Outline each blood parasite and name the species.
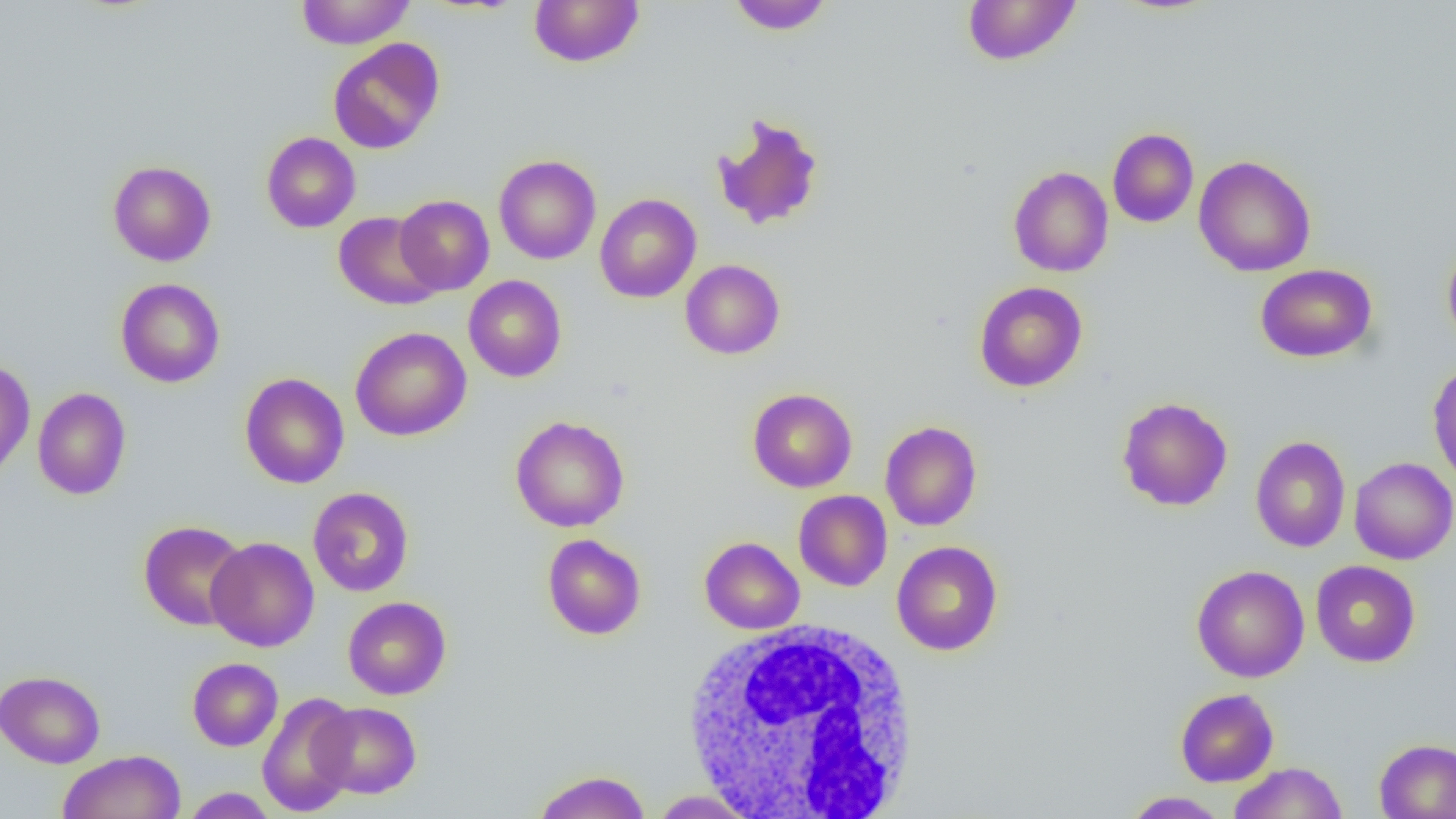
No blood parasites observed.

Summary:
  - Coordinate format: approximate bounding boxes as named x1/y1/x2/y2 corners in pixels
  - Uninfected red blood cell locations: (x1=295, y1=0, x2=415, y2=49), (x1=528, y1=0, x2=645, y2=68), (x1=726, y1=0, x2=835, y2=35), (x1=961, y1=0, x2=1082, y2=66), (x1=327, y1=38, x2=445, y2=154), (x1=712, y1=113, x2=825, y2=231), (x1=1107, y1=128, x2=1199, y2=227), (x1=261, y1=132, x2=361, y2=233), (x1=493, y1=154, x2=601, y2=265), (x1=1193, y1=155, x2=1316, y2=277), (x1=108, y1=161, x2=216, y2=266), (x1=1008, y1=166, x2=1113, y2=277), (x1=595, y1=194, x2=701, y2=303), (x1=394, y1=195, x2=494, y2=295), (x1=334, y1=212, x2=442, y2=310), (x1=1442, y1=241, x2=1456, y2=354), (x1=680, y1=259, x2=785, y2=359), (x1=1254, y1=263, x2=1378, y2=363), (x1=464, y1=275, x2=567, y2=382), (x1=115, y1=278, x2=225, y2=388), (x1=974, y1=281, x2=1088, y2=392), (x1=350, y1=326, x2=471, y2=441), (x1=0, y1=359, x2=35, y2=481), (x1=1427, y1=361, x2=1456, y2=491), (x1=239, y1=372, x2=349, y2=489), (x1=32, y1=388, x2=131, y2=500), (x1=748, y1=388, x2=857, y2=493), (x1=1116, y1=396, x2=1233, y2=512), (x1=510, y1=415, x2=630, y2=532), (x1=880, y1=421, x2=982, y2=531), (x1=1250, y1=435, x2=1351, y2=553), (x1=1349, y1=457, x2=1456, y2=565), (x1=308, y1=487, x2=414, y2=597), (x1=793, y1=490, x2=892, y2=591), (x1=138, y1=521, x2=249, y2=631), (x1=542, y1=534, x2=646, y2=639), (x1=206, y1=536, x2=319, y2=652), (x1=699, y1=537, x2=805, y2=634), (x1=891, y1=540, x2=1003, y2=656), (x1=1310, y1=560, x2=1420, y2=667), (x1=1192, y1=564, x2=1310, y2=682), (x1=343, y1=596, x2=451, y2=700), (x1=187, y1=657, x2=283, y2=751), (x1=0, y1=670, x2=105, y2=768), (x1=1175, y1=688, x2=1279, y2=787), (x1=257, y1=691, x2=359, y2=817), (x1=312, y1=702, x2=422, y2=799), (x1=1374, y1=738, x2=1456, y2=819), (x1=58, y1=750, x2=186, y2=819), (x1=1228, y1=762, x2=1348, y2=819), (x1=532, y1=770, x2=651, y2=819), (x1=180, y1=787, x2=278, y2=818), (x1=648, y1=789, x2=761, y2=818), (x1=1121, y1=791, x2=1230, y2=818)
  - White blood cell locations: (x1=682, y1=617, x2=922, y2=816)
  - Slide-level diagnosis: no evidence of blood parasites
  - Field of view: single
  - Magnification: 1000x
  - Preparation: thin blood smear
  - Image size: 1456×819 pixels
  - Modality: light microscopy